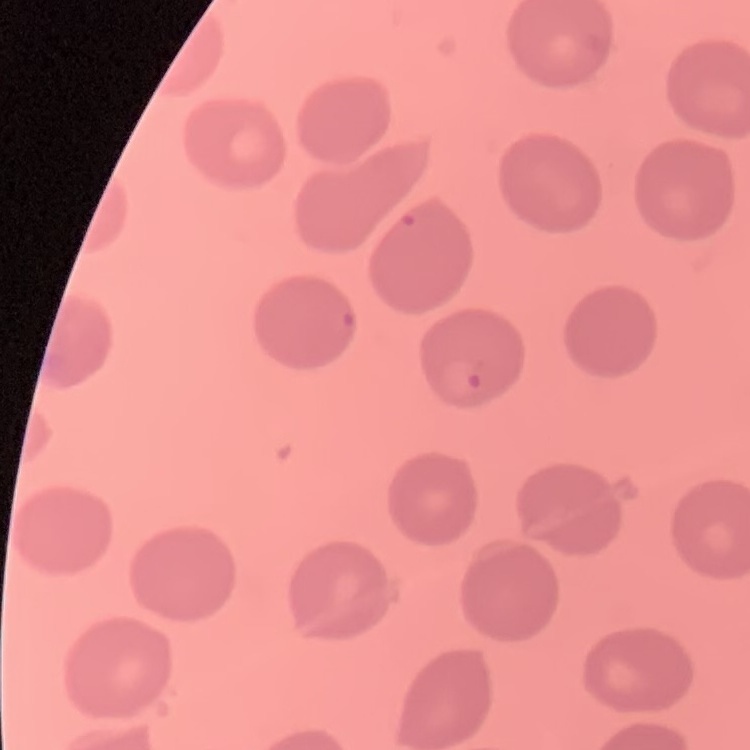
Summary:
  - Erythrocyte morphology: no rouleaux formation
  - Stain: Field's or Giemsa
  - Image type: one tile cut from a larger photomicrograph
  - Preparation: thin blood smear